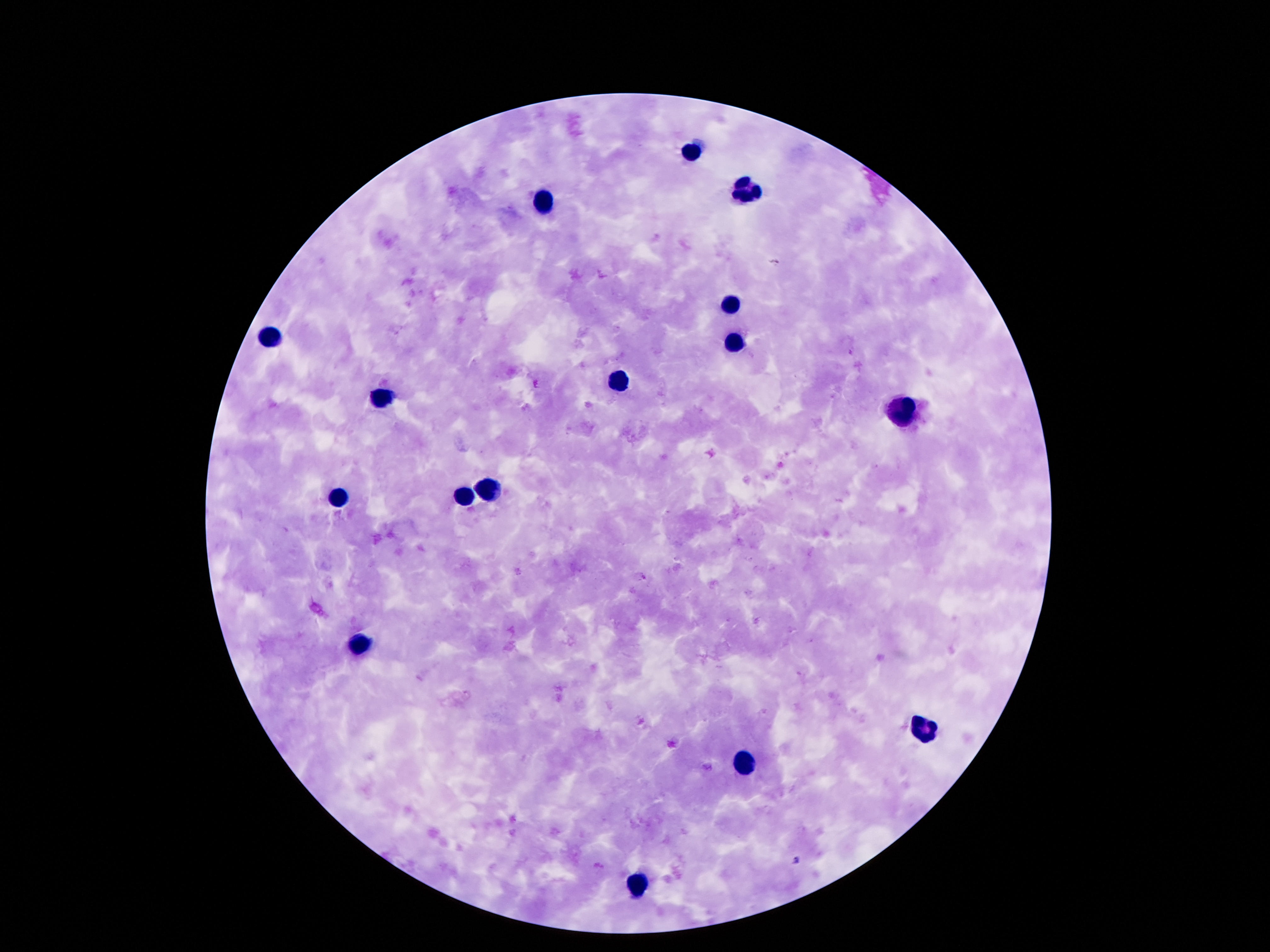

Approximate centers as {x, y} in pixels.
Summary:
  - Leukocyte locations: {692, 151}, {750, 193}, {544, 203}, {730, 307}, {270, 335}, {736, 345}, {616, 381}, {378, 395}, {900, 415}, {490, 491}, {466, 495}, {338, 500}, {358, 642}, {930, 730}, {744, 760}, {636, 886}
  - Stain: Giemsa
  - Image size: 1270×952 pixels
  - Preparation: thick blood smear
  - Field of view: one from this slide
  - Capture: smartphone camera through the microscope eyepiece
  - Magnification: 100x
  - Patient malaria status: negative